Classify this cell by malaria status.
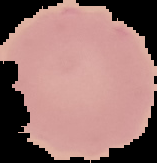
Uninfected.

preparation = thin blood smear
image type = cell region segmented out of the field of view; surrounding area masked to black
image size = 157×163 pixels